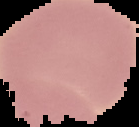
Summary:
  - Preparation: thin blood smear
  - Image type: segmented cell region on a black background
  - Image size: 139×127 pixels
  - Malaria status: uninfected